Locate and identify every blood parasite.
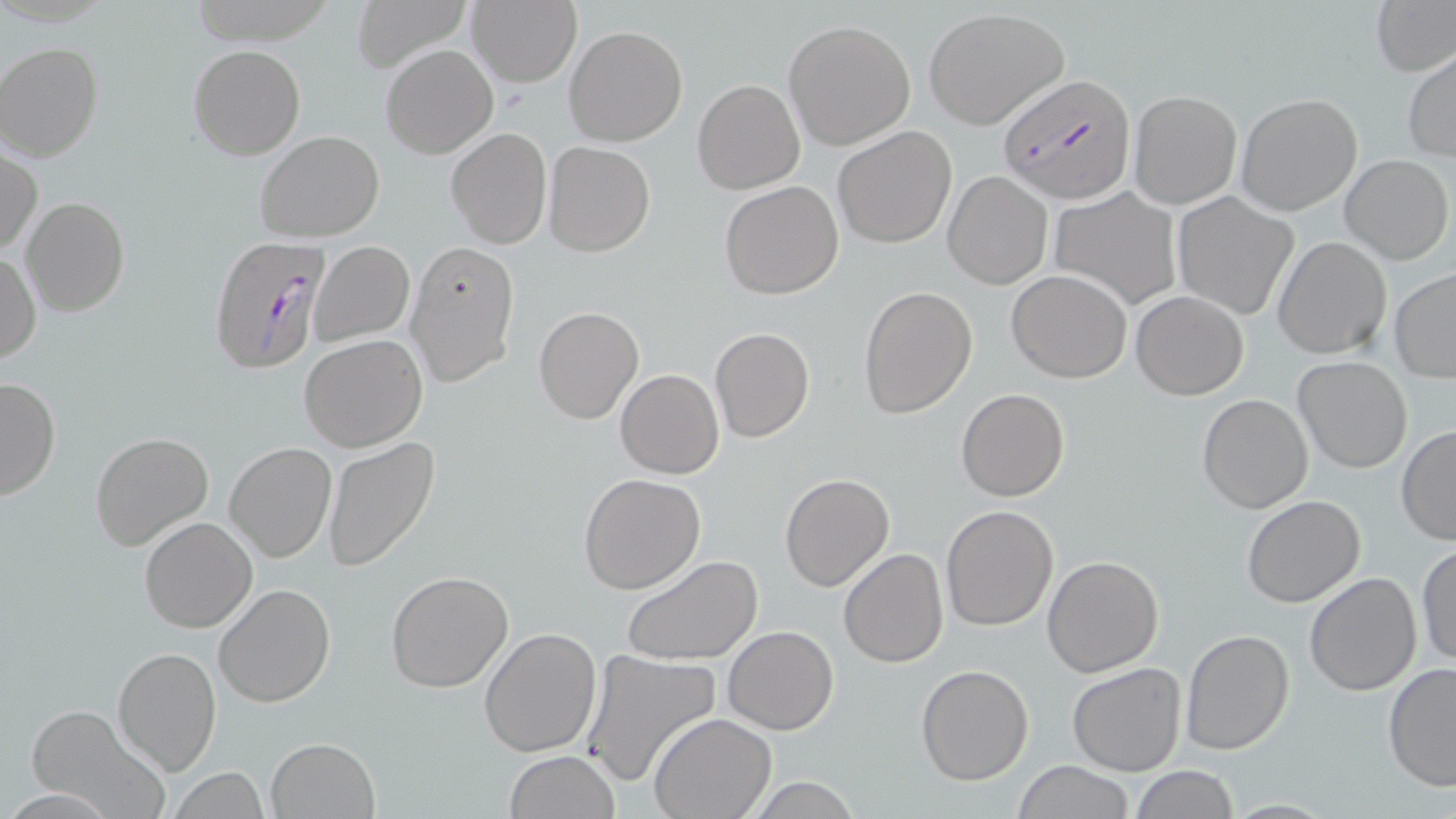
Approximate bounding boxes as (x1,y1)-(x2,y2) corner pairs in pixels.
Plasmodium falciparum-infected red blood cells: (996,72)-(1133,202), (208,235)-(333,374).
No Plasmodium ovale, Plasmodium malariae, Plasmodium vivax, Babesia divergens, or Trypanosoma brucei observed.

slide-level diagnosis = Plasmodium falciparum
modality = light microscopy
uninfected red blood cell locations = approximate bounding boxes as (x1,y1)-(x2,y2) corner pairs in pixels: (352,0)-(468,72), (468,0)-(582,88), (1372,0)-(1455,76), (924,8)-(1067,129), (783,19)-(915,150), (564,25)-(689,147), (0,42)-(104,162), (189,44)-(306,160), (382,44)-(497,159), (1404,50)-(1456,161), (692,79)-(805,195), (1128,90)-(1242,209), (1236,93)-(1362,215), (833,127)-(957,249), (446,128)-(552,248), (254,131)-(384,241), (543,141)-(657,257), (1,146)-(42,257), (1339,155)-(1452,264), (944,171)-(1052,288), (719,181)-(843,299), (1049,188)-(1181,311), (1172,191)-(1300,322), (21,198)-(131,318), (1273,237)-(1391,359), (309,240)-(414,348), (405,241)-(519,387), (1,249)-(40,366), (1390,268)-(1456,380), (1008,269)-(1131,383), (858,285)-(978,418), (1131,290)-(1249,400), (534,306)-(643,424), (709,327)-(814,444), (298,334)-(427,452), (1294,356)-(1413,473), (615,369)-(724,478), (0,374)-(60,502), (956,388)-(1070,502), (1196,393)-(1315,513), (1396,426)-(1456,545), (90,431)-(214,550), (322,437)-(442,572), (224,442)-(337,564), (578,473)-(707,594), (779,473)-(894,592), (1241,494)-(1366,607), (939,504)-(1059,632), (139,516)-(258,633), (1416,542)-(1456,668), (839,547)-(949,668), (622,554)-(763,666), (1042,555)-(1164,676), (386,571)-(514,693), (1303,572)-(1423,696), (214,583)-(335,708), (723,625)-(839,735), (479,627)-(601,758), (1181,628)-(1293,755), (113,646)-(223,776), (580,649)-(723,789), (1382,662)-(1456,791), (1067,663)-(1187,777), (916,664)-(1034,783), (27,708)-(163,811), (648,713)-(776,819), (266,737)-(379,818), (503,750)-(619,819), (1013,759)-(1134,819), (1129,766)-(1239,819), (168,767)-(269,819), (741,777)-(864,817)
preparation = thin blood film
stain = May-Grünwald-Giemsa
field of view = one of a larger specimen
magnification = 1000x
image size = 1456×819 pixels